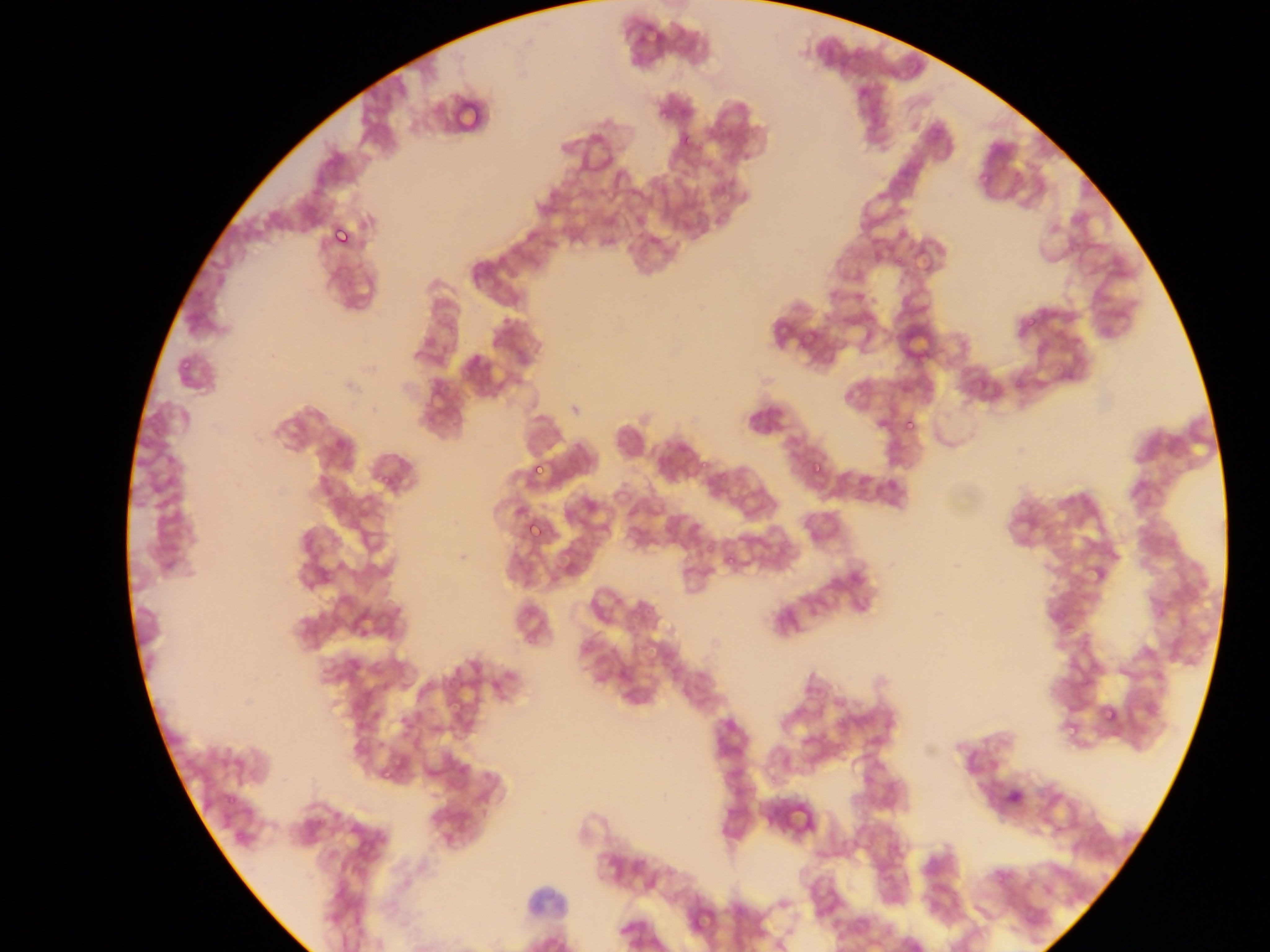

image size = 1270×952 pixels
malaria parasite locations = approximate bounding boxes as left top right bottom in pixels: 455 104 484 131; 658 108 675 123; 676 133 697 148; 973 168 994 185; 327 220 359 253; 1023 320 1036 331; 175 358 196 371; 901 414 923 438; 806 458 826 479; 528 459 549 482; 371 469 399 489; 523 517 546 542; 559 554 581 580; 725 556 735 571; 1079 565 1105 586; 1101 706 1120 726; 1058 723 1077 740; 378 770 393 785
country = Ghana
preparation = thin blood film
capture = mobile-phone photograph through a microscope
field of view = single